Report the malaria status of this cell.
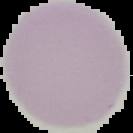
Uninfected.

image_type: segmented cell region with the area outside set to black
preparation: thin blood smear
image_size: 133×133 pixels